Assess this cell for malaria.
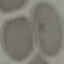
It is uninfected.

Thin smear of blood. Automatically extracted cell patch, resized to 64 × 64 pixels. Acquired by smartphone through the microscope eyepiece. Giemsa-stained preparation.